Give the position of every malaria parasite.
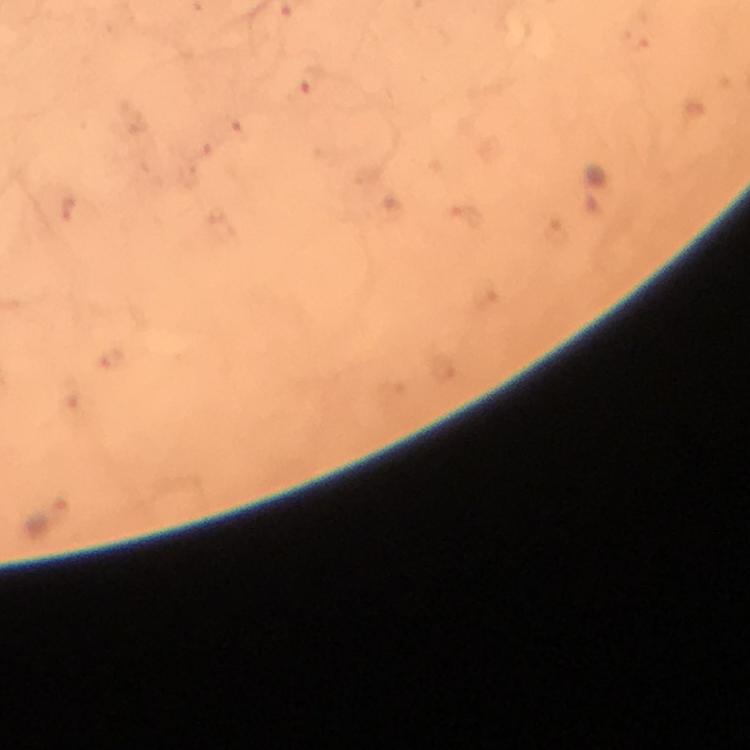
Approximate centers as [x, y] in pixels.
Malaria parasites: [311, 82], [70, 207].

A crop from one field of view. Giemsa-stained preparation. From a diagnostic examination for malaria. Immersion oil was used. 100x magnification. Thick smear. Image is 750×750 pixels. Photographed with a smartphone mounted on the microscope.